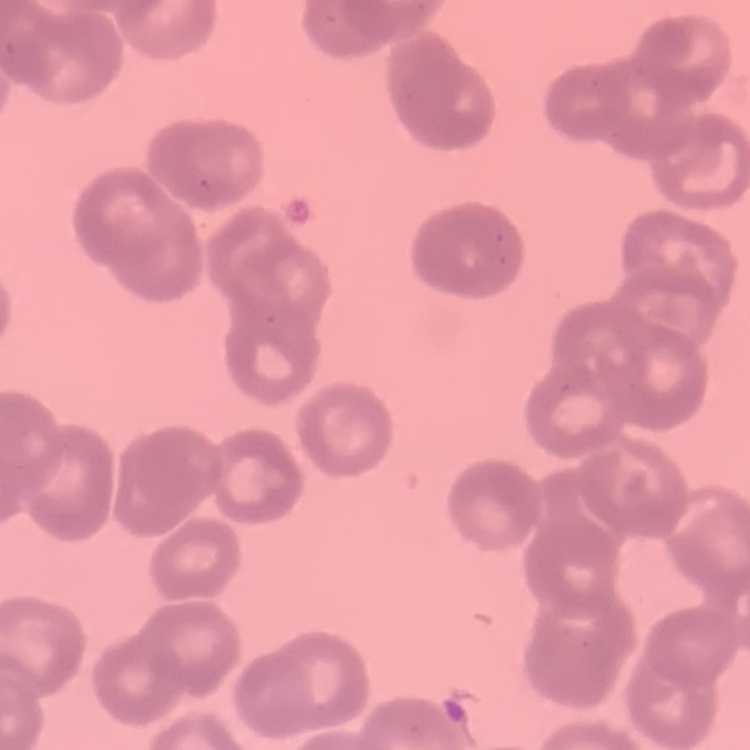

Summary:
  - Red blood cell morphology: rouleaux formation
  - Stain: Field's or Giemsa
  - Image type: one tile cut from a larger photomicrograph
  - Preparation: thin blood smear